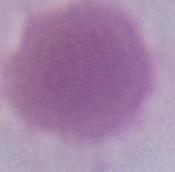
Summary:
  - Identification: erythrocyte
  - Magnification: 1000x
  - Modality: micrograph